State the preparation type.
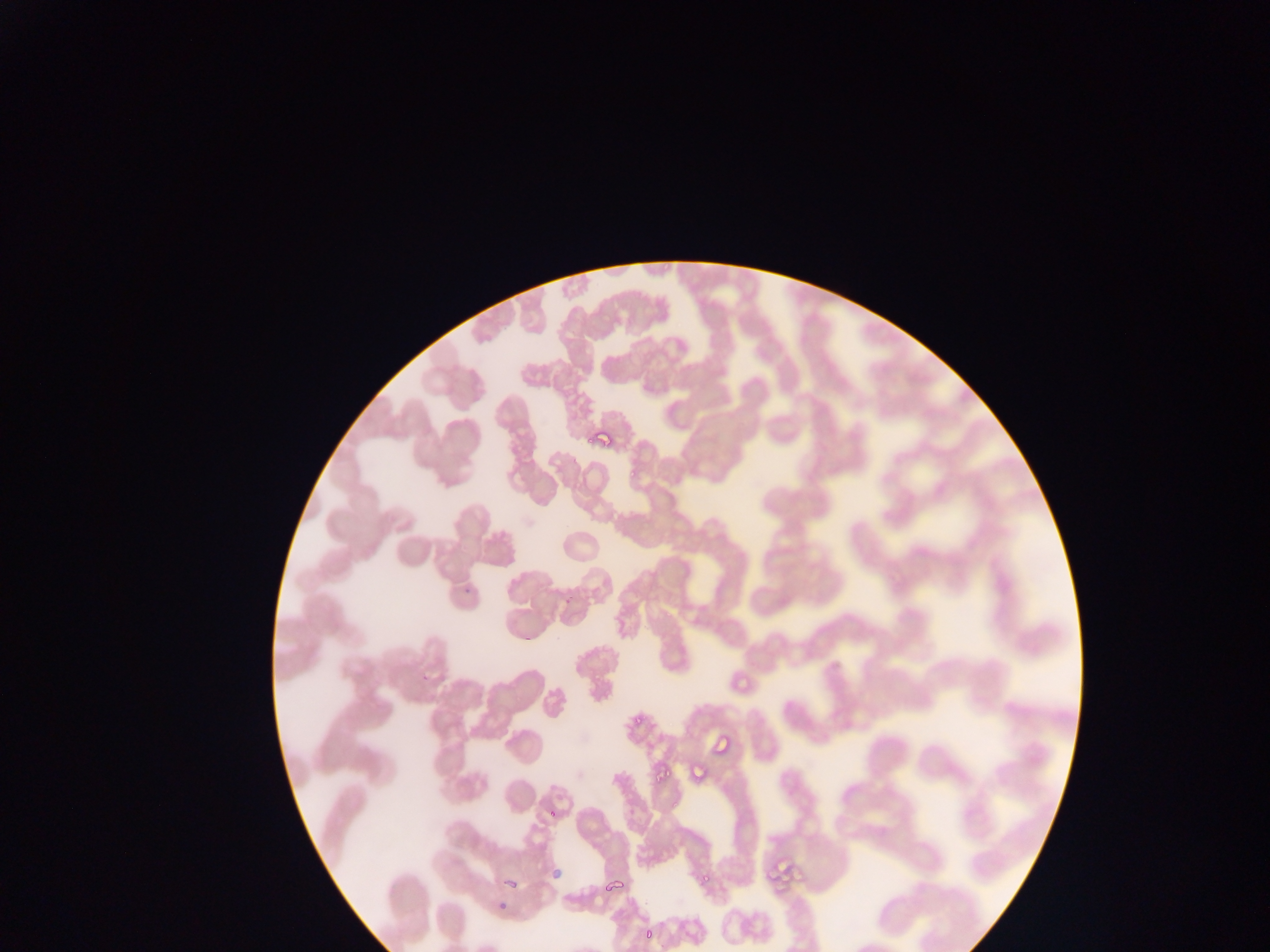

This is a thin smear.

Approximate bounding boxes as (left, top, right, bottom) in pixels.
Summary:
  - Plasmodium parasite locations: (589, 427, 611, 452), (730, 666, 754, 692), (709, 731, 738, 763), (692, 763, 709, 782), (768, 849, 827, 894), (555, 864, 561, 884), (496, 869, 526, 894), (598, 871, 629, 893), (496, 895, 518, 920), (643, 921, 660, 946)
  - Capture: mobile-phone photograph through a microscope
  - Field of view: single
  - Country: Ghana
  - Image size: 1270×952 pixels